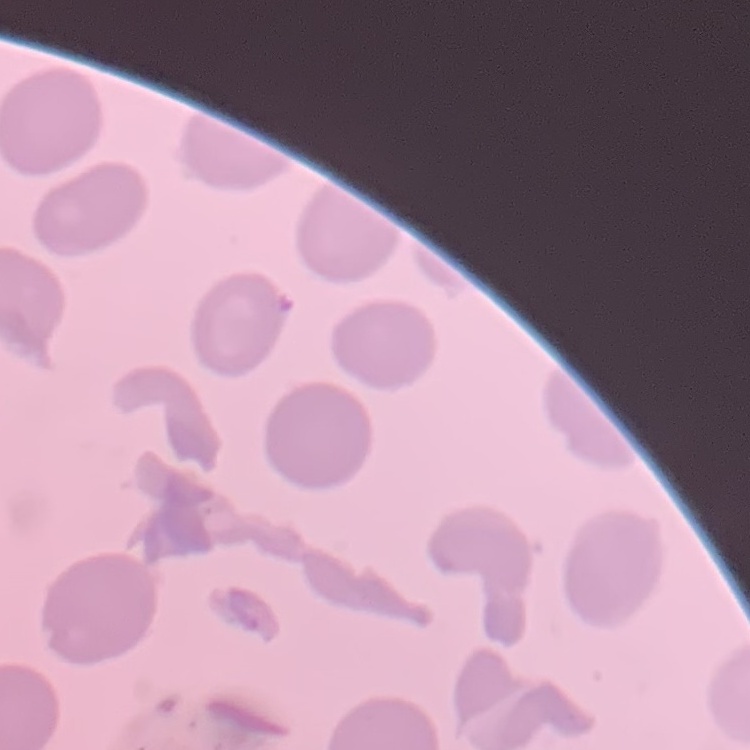 The red blood cells exhibit no rouleaux formation. Stained with either Field's or Giemsa. Thin blood smear. One tile cut from a larger photomicrograph.